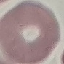
malaria status = uninfected
stain = Giemsa
preparation = thin blood smear
image type = automatically extracted cell patch, resized to 64 × 64 pixels
capture = smartphone through the microscope eyepiece